Outline each Plasmodium parasite.
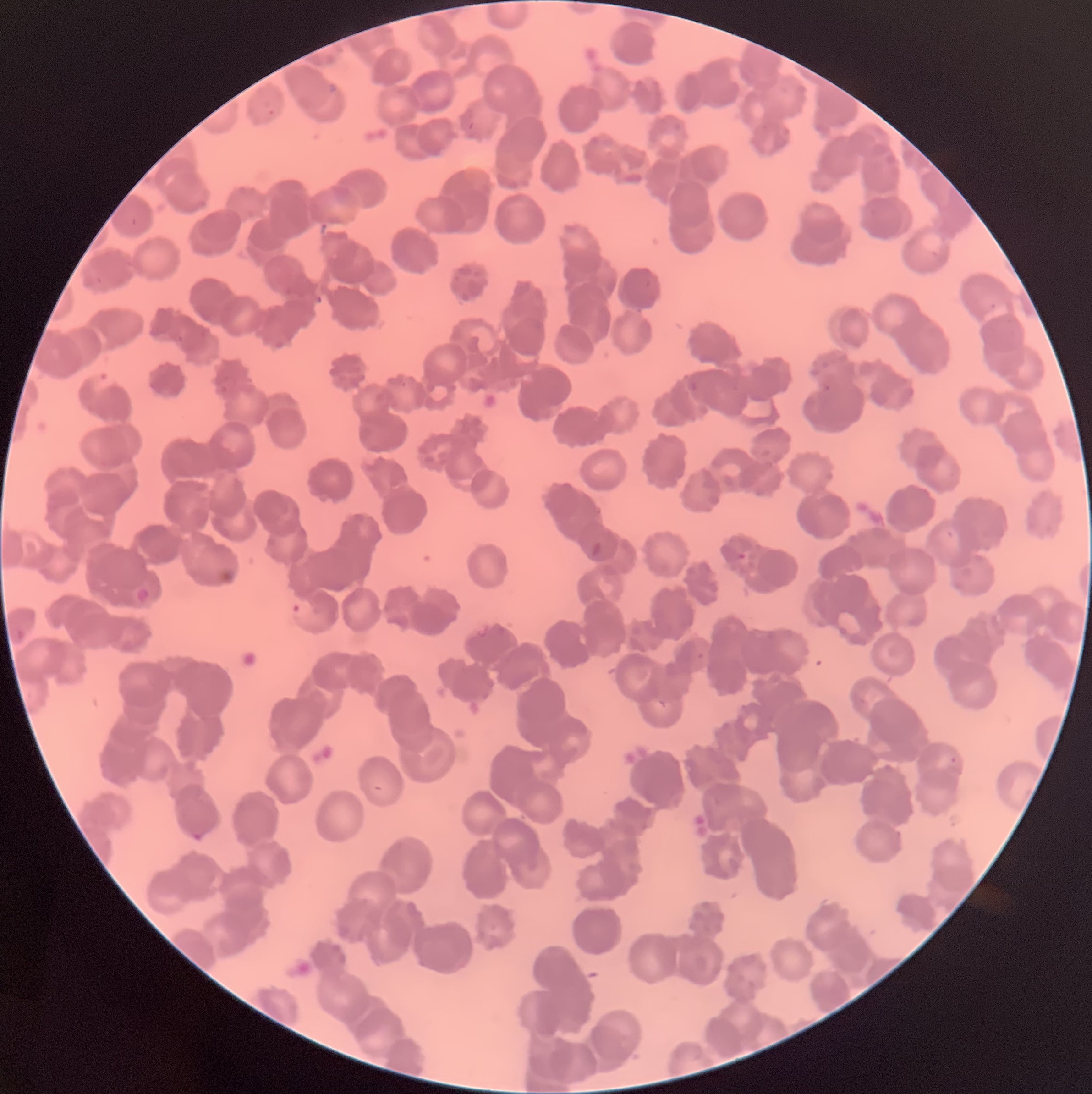

Approximate bounding boxes as [x1, y1, x2, y2] in pixels.
Plasmodium parasites: [90, 372, 119, 388], [135, 588, 151, 605], [288, 599, 316, 620].

Summary:
  - Image size: 1092×1094 pixels
  - Modality: optical microscopy
  - Preparation: thin blood film
  - Red blood cell morphology: rouleaux formation